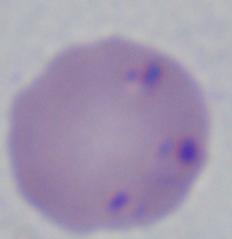

1000x magnification. Micrograph. A Babesia parasite is shown.